Assess the morphology of the red blood cells.
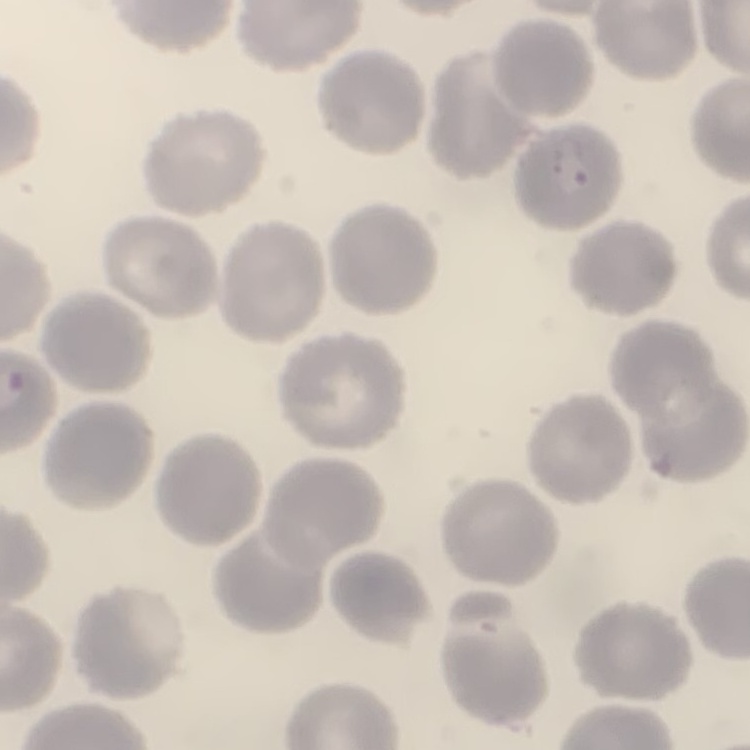
They show no rouleaux formation.

Summary:
  - Preparation: thin blood film
  - Stain: Field's or Giemsa
  - Image type: square crop of a larger photomicrograph